Name the blood parasite species.
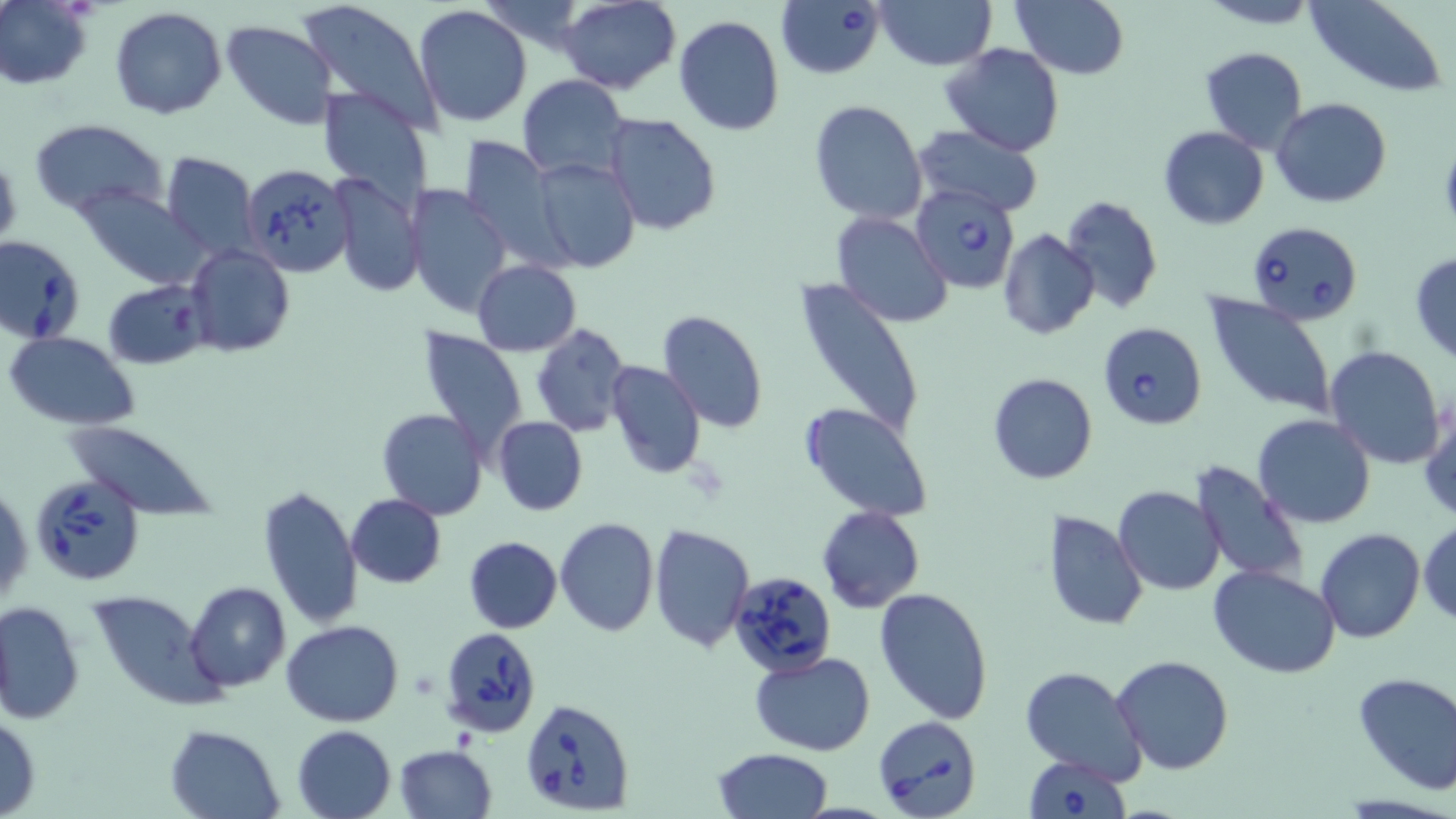

Babesia divergens.

Approximate bounding boxes as (x1,y1)-(x2,y2) corner pairs in pixels. Uninfected red blood cell locations: (0,0)-(92,90), (557,0)-(681,92), (1011,0)-(1131,79), (1200,0)-(1319,29), (1306,0)-(1448,95), (295,1)-(441,133), (477,1)-(587,49), (876,1)-(996,71), (412,4)-(533,128), (109,6)-(227,120), (674,15)-(786,137), (221,19)-(340,129), (941,42)-(1065,157), (1200,46)-(1309,153), (517,73)-(629,181), (317,86)-(434,212), (1270,98)-(1392,208), (808,99)-(927,225), (602,112)-(722,237), (29,118)-(169,220), (912,126)-(1043,218), (1158,126)-(1269,230), (459,136)-(570,271), (159,151)-(259,262), (532,156)-(639,272), (330,174)-(424,297), (75,185)-(212,290), (407,185)-(513,320), (1060,194)-(1164,315), (830,211)-(952,328), (998,229)-(1099,341), (185,245)-(294,357), (1409,252)-(1456,363), (472,259)-(582,355), (794,279)-(925,443), (103,280)-(209,369), (1202,294)-(1338,420), (657,310)-(767,432), (531,323)-(631,438), (418,327)-(531,458), (5,331)-(139,429), (1324,345)-(1446,469), (605,360)-(706,479), (987,372)-(1097,485), (801,402)-(933,520), (1420,402)-(1455,523), (376,408)-(489,521), (1252,415)-(1376,529), (493,416)-(587,515), (61,420)-(215,515), (1268,429)-(1391,601), (1191,461)-(1309,588), (1,480)-(32,608), (258,486)-(362,629), (1114,487)-(1224,596), (345,493)-(446,589), (816,506)-(925,612), (1043,510)-(1149,632), (555,518)-(659,637), (1418,518)-(1456,626), (649,522)-(754,652), (1315,528)-(1426,643), (463,535)-(562,633), (1209,565)-(1340,678), (187,581)-(292,691), (874,586)-(994,725), (89,591)-(224,710), (0,598)-(84,725), (282,618)-(403,727), (750,652)-(877,756), (1112,654)-(1235,774), (1020,665)-(1148,785), (1351,671)-(1456,795), (0,712)-(40,819), (164,724)-(285,818), (292,725)-(397,818), (393,744)-(497,818), (712,747)-(833,819). Babesia divergens-infected red blood cell locations: (777,1)-(886,80), (240,162)-(354,276), (913,184)-(1022,295), (1248,220)-(1362,326), (0,234)-(85,344), (1098,323)-(1206,430), (29,472)-(145,586), (729,569)-(836,677), (440,629)-(543,742), (520,699)-(635,815), (873,714)-(983,819), (1024,754)-(1131,818). Captured at 1000x magnification. Image is 1456×819 pixels. May-Grünwald-Giemsa stain. Light microscopy. One field of a larger specimen. Thin blood smear.